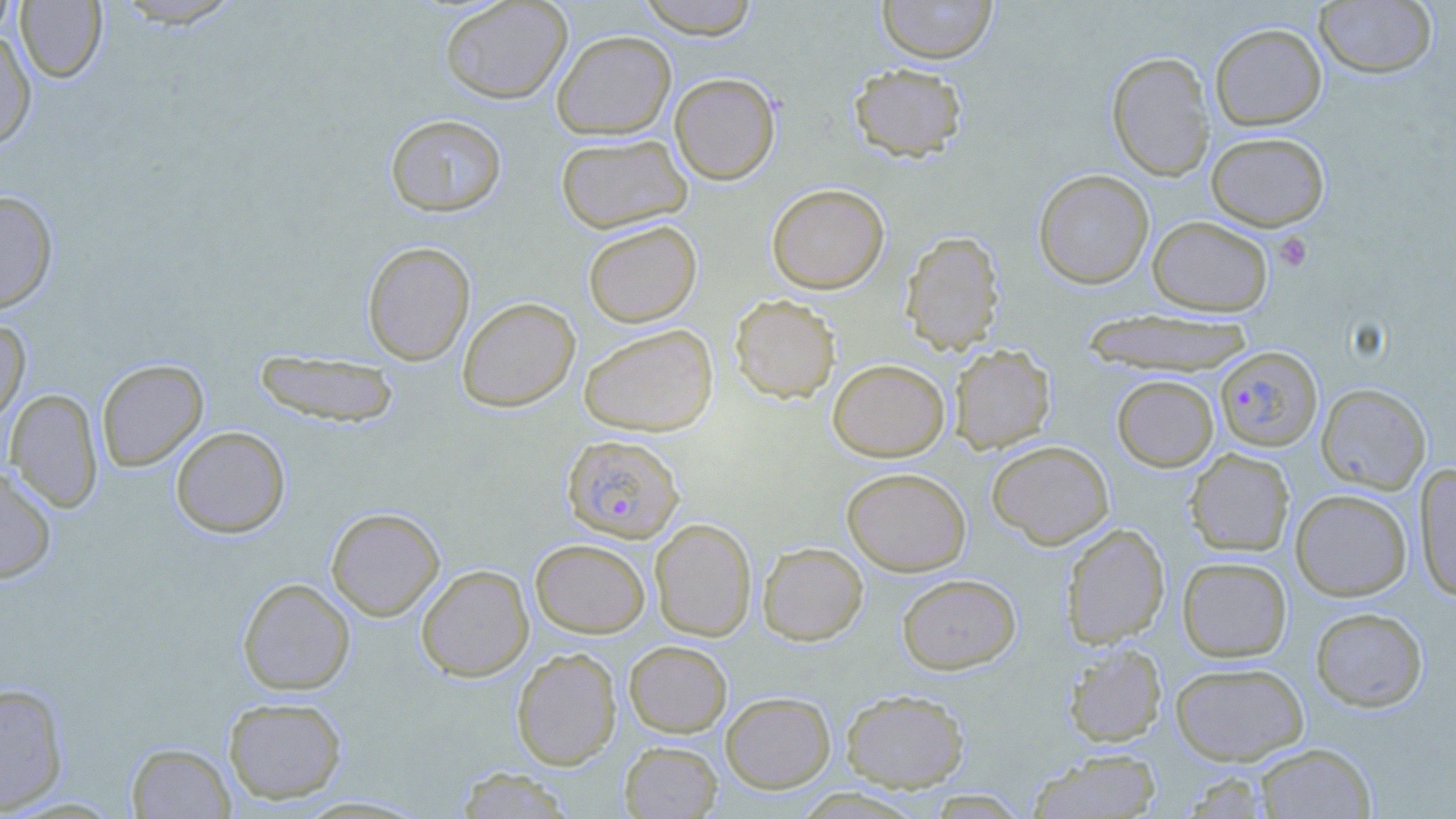

Plasmodium falciparum-infected red blood cell locations = approximate bounding boxes as [x1, y1, x2, y2] in pixels: [1215, 346, 1322, 452], [561, 434, 684, 543]
slide-level diagnosis = Plasmodium falciparum
stain = May-Grünwald-Giemsa
preparation = thin blood film
platelet locations = approximate bounding boxes as [x1, y1, x2, y2] in pixels: [1273, 232, 1312, 272]
image size = 1456×819 pixels
modality = light microscopy
field of view = one of a larger specimen
magnification = 1000x
uninfected red blood cell locations = approximate bounding boxes as [x1, y1, x2, y2] in pixels: [0, 0, 16, 43], [109, 0, 246, 28], [439, 0, 573, 104], [635, 0, 761, 39], [876, 0, 998, 64], [1314, 0, 1438, 78], [14, 1, 107, 83], [1210, 23, 1327, 131], [0, 30, 36, 150], [551, 30, 676, 140], [1106, 51, 1215, 181], [848, 63, 968, 162], [669, 72, 781, 185], [385, 113, 507, 217], [1206, 132, 1330, 231], [556, 134, 693, 234], [1033, 169, 1154, 289], [767, 183, 890, 294], [0, 189, 58, 314], [1147, 216, 1273, 316], [582, 220, 702, 328], [900, 231, 1004, 355], [362, 241, 475, 365], [730, 294, 841, 403], [457, 296, 580, 412], [1081, 308, 1255, 377], [0, 319, 31, 424], [578, 323, 718, 436], [949, 344, 1055, 454], [254, 350, 401, 428], [96, 359, 208, 471], [828, 359, 949, 462], [1112, 375, 1219, 472], [1316, 383, 1431, 493], [5, 389, 104, 512], [170, 426, 290, 538], [986, 440, 1114, 549], [1185, 449, 1295, 556], [1415, 463, 1456, 603], [0, 466, 57, 584], [841, 467, 971, 576], [1290, 489, 1412, 601], [326, 506, 445, 621], [649, 518, 757, 641], [1060, 523, 1170, 648], [530, 538, 650, 638], [757, 541, 868, 646], [1177, 556, 1292, 662], [416, 564, 534, 682], [897, 573, 1021, 674], [237, 577, 356, 695], [1310, 607, 1428, 712], [624, 640, 732, 737], [1063, 642, 1167, 747], [511, 647, 622, 770], [1170, 661, 1309, 765], [0, 682, 69, 815], [841, 688, 969, 792], [720, 691, 835, 793], [223, 696, 348, 804], [620, 741, 722, 818], [126, 743, 235, 818], [1255, 743, 1376, 818], [1029, 749, 1163, 819], [454, 766, 576, 818], [1179, 770, 1274, 818]